Report the malaria status of this cell.
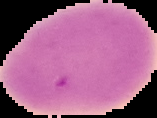

Uninfected.

Summary:
  - Image type: cell region segmented out of the field of view; surrounding area masked to black
  - Preparation: thin blood smear
  - Image size: 157×118 pixels